Report the malaria status of this cell.
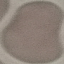

It is uninfected.

Cell patch, automatically extracted from a larger field of view and resized to 64 × 64 pixels. Acquired by smartphone through the microscope eyepiece. Giemsa-stained preparation. Thin smear of blood.